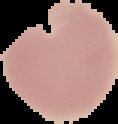

preparation: thin blood smear
malaria_status: uninfected
image_size: 118×124 pixels
image_type: cell region segmented out of the field of view; surrounding area masked to black